Point out every malaria parasite.
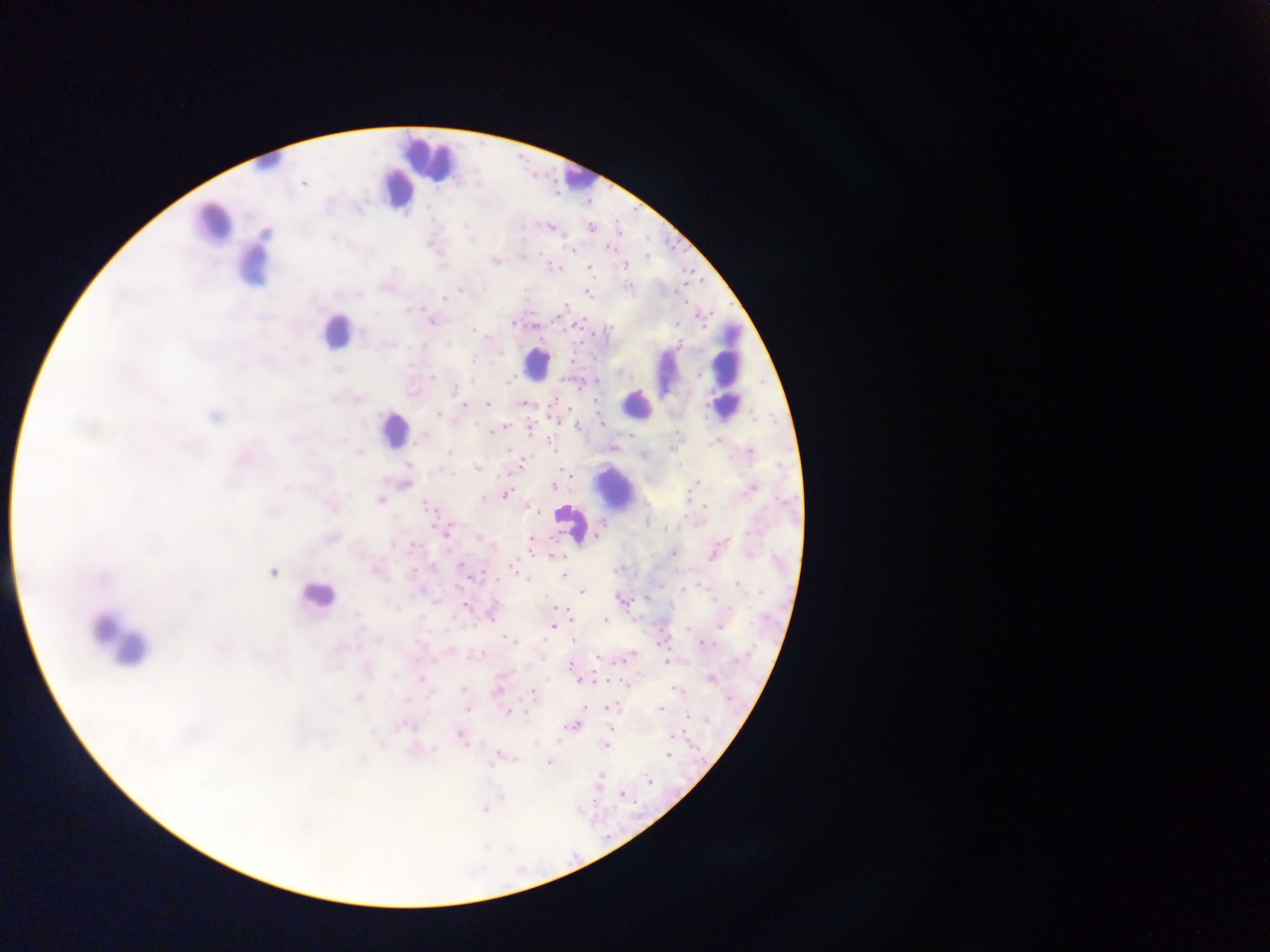
Approximate centers as (x, y) in pixels.
Malaria parasites: (304, 183), (465, 225), (551, 228), (591, 228), (266, 233), (471, 240), (608, 247), (572, 250), (647, 257), (494, 261), (624, 266), (589, 267), (554, 268), (627, 286), (484, 288), (459, 289), (587, 293), (443, 298), (564, 306), (407, 309), (431, 321), (512, 323), (678, 323), (576, 324), (535, 325), (610, 328), (473, 330), (363, 331), (679, 344), (448, 345), (473, 361), (410, 364), (339, 370), (700, 375), (433, 378), (509, 380), (454, 388), (553, 401), (487, 404), (465, 405), (523, 405), (438, 414), (214, 416), (601, 423), (502, 427), (577, 427), (530, 428), (492, 432), (424, 438), (551, 442), (717, 442), (613, 446), (510, 450), (359, 452), (751, 452), (449, 453), (409, 465), (521, 465), (477, 469), (697, 482), (406, 485), (554, 487), (751, 488), (505, 494), (483, 499), (380, 500), (426, 505), (704, 506), (332, 508), (532, 508), (665, 529), (446, 532), (330, 538), (531, 539), (156, 544), (413, 546), (673, 554), (749, 555), (554, 557), (461, 565), (433, 568), (513, 568), (273, 572), (378, 573), (564, 574), (738, 585), (685, 588), (582, 592), (619, 599), (433, 602), (465, 606), (728, 609), (492, 612), (358, 615), (605, 620), (554, 626), (719, 626), (176, 628), (688, 628), (378, 639), (509, 640), (574, 640), (704, 644), (480, 654), (631, 655), (598, 657), (666, 663), (570, 665), (366, 671), (395, 676), (710, 678), (421, 679), (579, 680), (463, 689), (675, 689), (497, 691), (430, 693), (532, 693), (357, 698), (728, 699), (585, 707), (609, 707), (467, 709), (660, 709), (509, 713), (688, 715), (706, 720), (405, 726), (572, 726), (672, 735), (461, 736), (536, 744), (606, 746), (434, 749), (668, 755), (514, 758), (496, 759), (549, 762), (489, 766), (600, 777), (649, 781), (623, 795), (502, 797), (484, 809).

leukocyte locations = approximate centers as (x, y) in pixels: (427, 158), (264, 165), (575, 177), (396, 188), (213, 223), (253, 267), (335, 330), (728, 355), (535, 363), (665, 373), (726, 396), (636, 405), (394, 428), (614, 487), (572, 523), (316, 595), (120, 644)
image size = 1270×952 pixels
capture = mobile-phone photograph through a microscope
field of view = single
preparation = thick blood smear
country = Ghana